State which parasite is depicted.
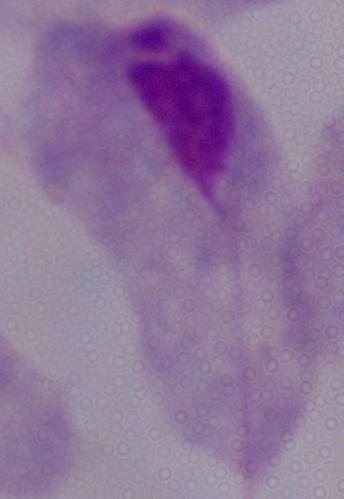
A trichomonad.

{
  "modality": "micrograph",
  "magnification": "1000x"
}